Outline each blood parasite and name the species.
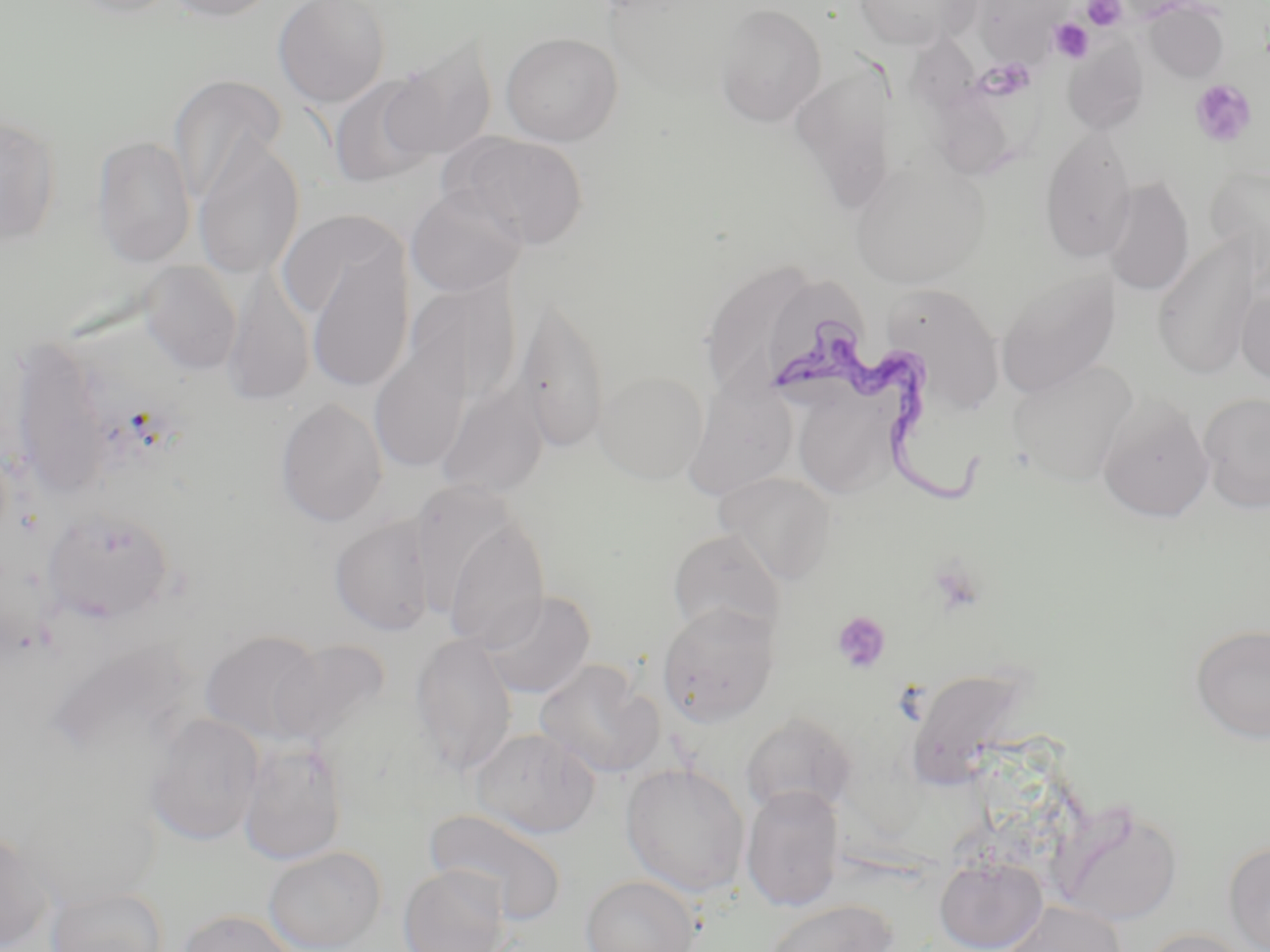

Approximate bounding boxes as named x1/y1/x2/y2 corners in pixels.
Trypanosoma brucei: (x1=769, y1=324, x2=987, y2=505).
No Plasmodium falciparum, Plasmodium ovale, Plasmodium malariae, Plasmodium vivax, or Babesia divergens observed.

{
  "slide_level_diagnosis": "Trypanosoma brucei",
  "field_of_view": "single",
  "platelet_locations": "approximate bounding boxes as named x1/y1/x2/y2 corners in pixels: (x1=1083, y1=0, x2=1126, y2=30), (x1=1049, y1=18, x2=1094, y2=63), (x1=1190, y1=79, x2=1257, y2=148), (x1=927, y1=556, x2=988, y2=617), (x1=832, y1=611, x2=891, y2=674)",
  "stain": "May-Grünwald-Giemsa",
  "uninfected_red_blood_cell_locations": "approximate bounding boxes as named x1/y1/x2/y2 corners in pixels: (x1=64, y1=0, x2=182, y2=19), (x1=161, y1=0, x2=279, y2=22), (x1=273, y1=0, x2=391, y2=107), (x1=853, y1=0, x2=980, y2=51), (x1=976, y1=0, x2=1069, y2=62), (x1=1144, y1=2, x2=1230, y2=83), (x1=715, y1=3, x2=827, y2=126), (x1=501, y1=31, x2=623, y2=146), (x1=382, y1=36, x2=498, y2=163), (x1=906, y1=39, x2=1025, y2=181), (x1=1063, y1=40, x2=1150, y2=135), (x1=793, y1=60, x2=904, y2=212), (x1=169, y1=74, x2=287, y2=206), (x1=328, y1=74, x2=440, y2=188), (x1=0, y1=112, x2=62, y2=246), (x1=1040, y1=129, x2=1137, y2=262), (x1=449, y1=132, x2=589, y2=249), (x1=92, y1=135, x2=196, y2=267), (x1=193, y1=136, x2=305, y2=279), (x1=850, y1=159, x2=988, y2=288), (x1=1205, y1=165, x2=1269, y2=270), (x1=1103, y1=176, x2=1194, y2=298), (x1=406, y1=186, x2=527, y2=297), (x1=278, y1=209, x2=407, y2=323), (x1=1152, y1=240, x2=1259, y2=380), (x1=306, y1=243, x2=415, y2=393), (x1=140, y1=260, x2=242, y2=376), (x1=704, y1=264, x2=816, y2=395), (x1=222, y1=272, x2=315, y2=407), (x1=996, y1=272, x2=1119, y2=399), (x1=404, y1=277, x2=522, y2=409), (x1=1236, y1=283, x2=1270, y2=388), (x1=886, y1=284, x2=1005, y2=415), (x1=517, y1=296, x2=610, y2=455), (x1=369, y1=333, x2=474, y2=473), (x1=8, y1=339, x2=116, y2=497), (x1=1008, y1=361, x2=1138, y2=485), (x1=594, y1=370, x2=709, y2=484), (x1=437, y1=381, x2=549, y2=502), (x1=683, y1=381, x2=797, y2=500), (x1=792, y1=388, x2=897, y2=499), (x1=1199, y1=391, x2=1270, y2=514), (x1=1097, y1=397, x2=1214, y2=522), (x1=275, y1=398, x2=388, y2=527), (x1=716, y1=472, x2=837, y2=583), (x1=41, y1=508, x2=176, y2=624), (x1=329, y1=514, x2=437, y2=636), (x1=442, y1=515, x2=551, y2=652), (x1=667, y1=529, x2=786, y2=640), (x1=479, y1=590, x2=596, y2=699), (x1=657, y1=603, x2=780, y2=727), (x1=1190, y1=623, x2=1270, y2=743), (x1=200, y1=630, x2=328, y2=745), (x1=409, y1=633, x2=517, y2=778), (x1=270, y1=639, x2=390, y2=748), (x1=533, y1=659, x2=664, y2=779), (x1=905, y1=665, x2=1034, y2=789), (x1=740, y1=712, x2=858, y2=817), (x1=146, y1=714, x2=264, y2=845), (x1=469, y1=727, x2=599, y2=839), (x1=238, y1=738, x2=348, y2=865), (x1=620, y1=762, x2=751, y2=898), (x1=741, y1=784, x2=845, y2=912), (x1=1052, y1=801, x2=1184, y2=926), (x1=424, y1=808, x2=568, y2=925), (x1=0, y1=827, x2=51, y2=952), (x1=1223, y1=840, x2=1270, y2=952), (x1=263, y1=846, x2=386, y2=952), (x1=934, y1=855, x2=1047, y2=952), (x1=398, y1=865, x2=511, y2=952), (x1=580, y1=875, x2=701, y2=952), (x1=45, y1=886, x2=168, y2=952), (x1=763, y1=899, x2=897, y2=952), (x1=999, y1=900, x2=1127, y2=952), (x1=177, y1=909, x2=297, y2=952), (x1=1141, y1=927, x2=1256, y2=952)",
  "modality": "optical microscopy",
  "preparation": "thin blood film",
  "magnification": "1000x",
  "image_size": "1270×952 pixels"
}